Assess this cell for malaria.
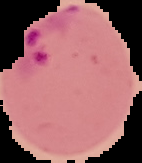

It is parasitized.

From a thin blood smear. Image is 142×163 pixels. The area outside the segmented cell region is set to black.